Point out Plasmodium parasites and leukocytes.
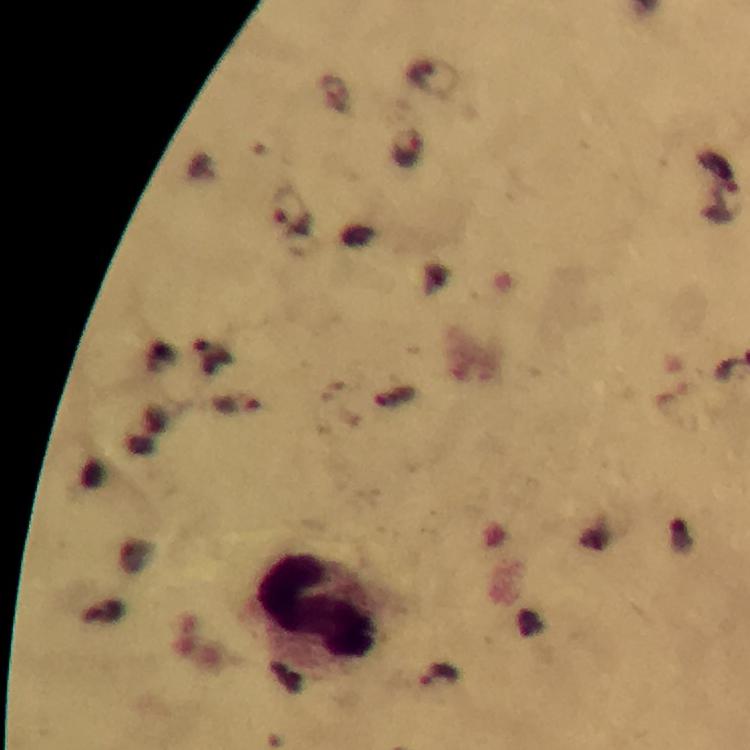

Approximate object centers, in pixels from the top-left corner.
Plasmodium parasites: (x=407, y=147), (x=292, y=211), (x=237, y=405), (x=438, y=677).
Leukocytes: (x=315, y=609).

Giemsa-stained preparation. 100x magnification. Immersion oil applied. Smartphone photograph taken through a microscope. A crop from one field of view. Image is 750×750 pixels. From a malaria diagnostic workup. Thick smear.